Describe the morphology of the red blood cells.
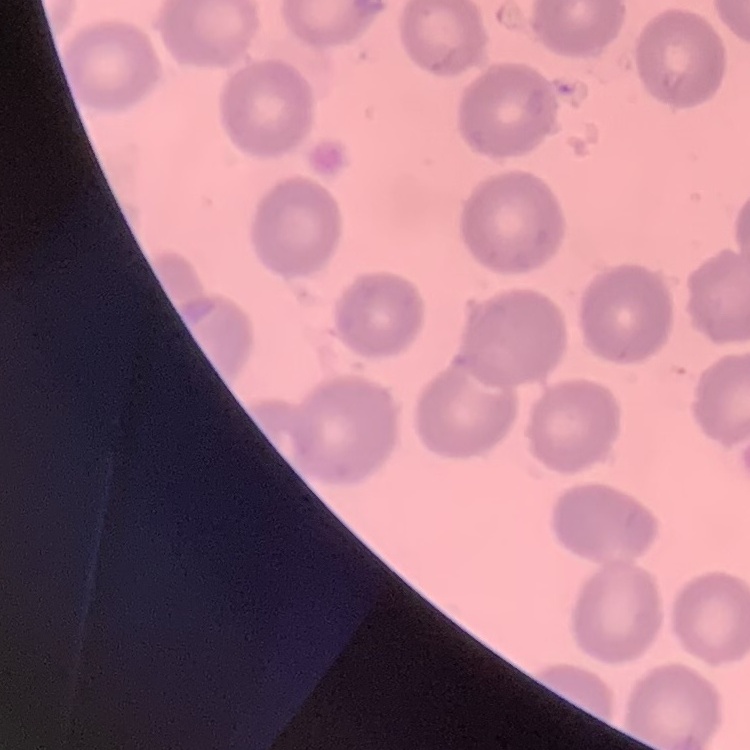

No rouleaux formation.

{
  "preparation": "thin peripheral smear",
  "image_type": "one tile cut from a larger photomicrograph",
  "stain": "Field's or Giemsa"
}